Report the malaria status of this cell.
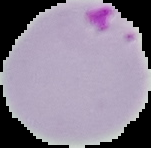
Parasitized.

Cell region segmented out of the field of view; the surrounding area is masked to black. From a thin blood smear. Image is 151×148 pixels.